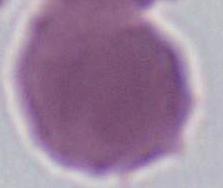
Summary:
  - Modality: micrograph
  - Identification: red blood cell
  - Magnification: 1000x